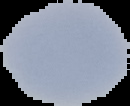 The area outside the segmented cell region is set to black. Image is 130×106 pixels. Result: no Plasmodium parasites detected. From a thin blood smear.